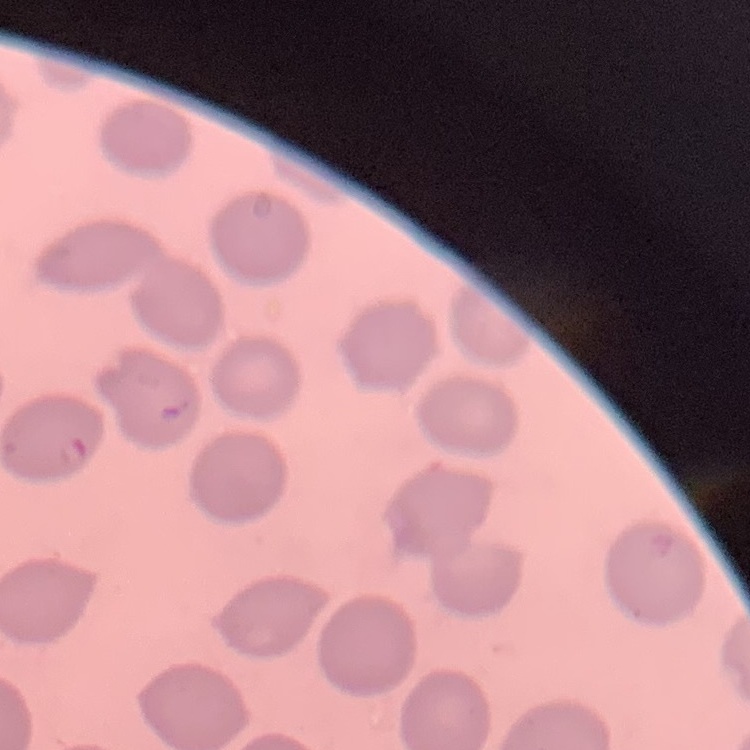
Summary:
  - Red blood cell morphology: no rouleaux formation
  - Preparation: thin peripheral smear
  - Stain: Field's or Giemsa
  - Image type: one tile cut from a larger photomicrograph